Classify this cell by malaria status.
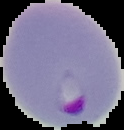
Parasitized.

Image is 124×130 pixels. From a thin blood smear. Segmented cell region on a black background.